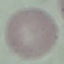
Summary:
  - Malaria status: uninfected
  - Preparation: thin blood film
  - Stain: Giemsa
  - Capture: smartphone camera at the microscope eyepiece
  - Image type: cell patch, automatically extracted from a larger field of view and resized to 64 × 64 pixels